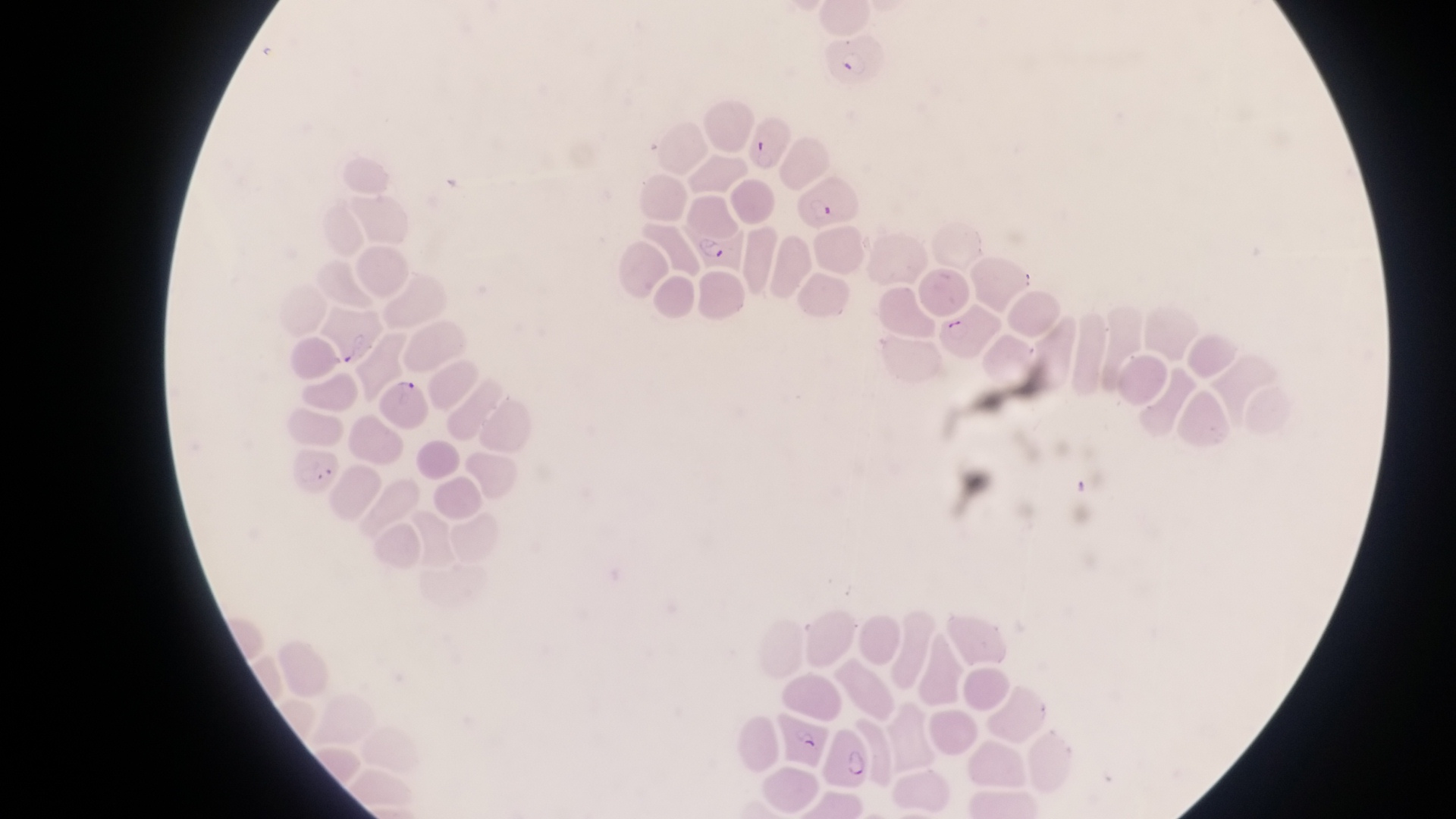

Approximate bounding boxes as left top right bottom in pixels. Parasitised red blood cell locations: 824 39 883 92; 740 116 789 176; 802 178 855 227; 684 218 750 274; 938 307 1005 357; 380 375 432 430; 288 438 343 498; 782 708 829 767; 829 727 874 790. At a magnification of 1000x. Thin blood film. Single field of view. Image is 1456×819 pixels. Captured by a smartphone held over the eyepiece of an Olympus CX-23 microscope. Sample from Uganda.